State the blood parasite species.
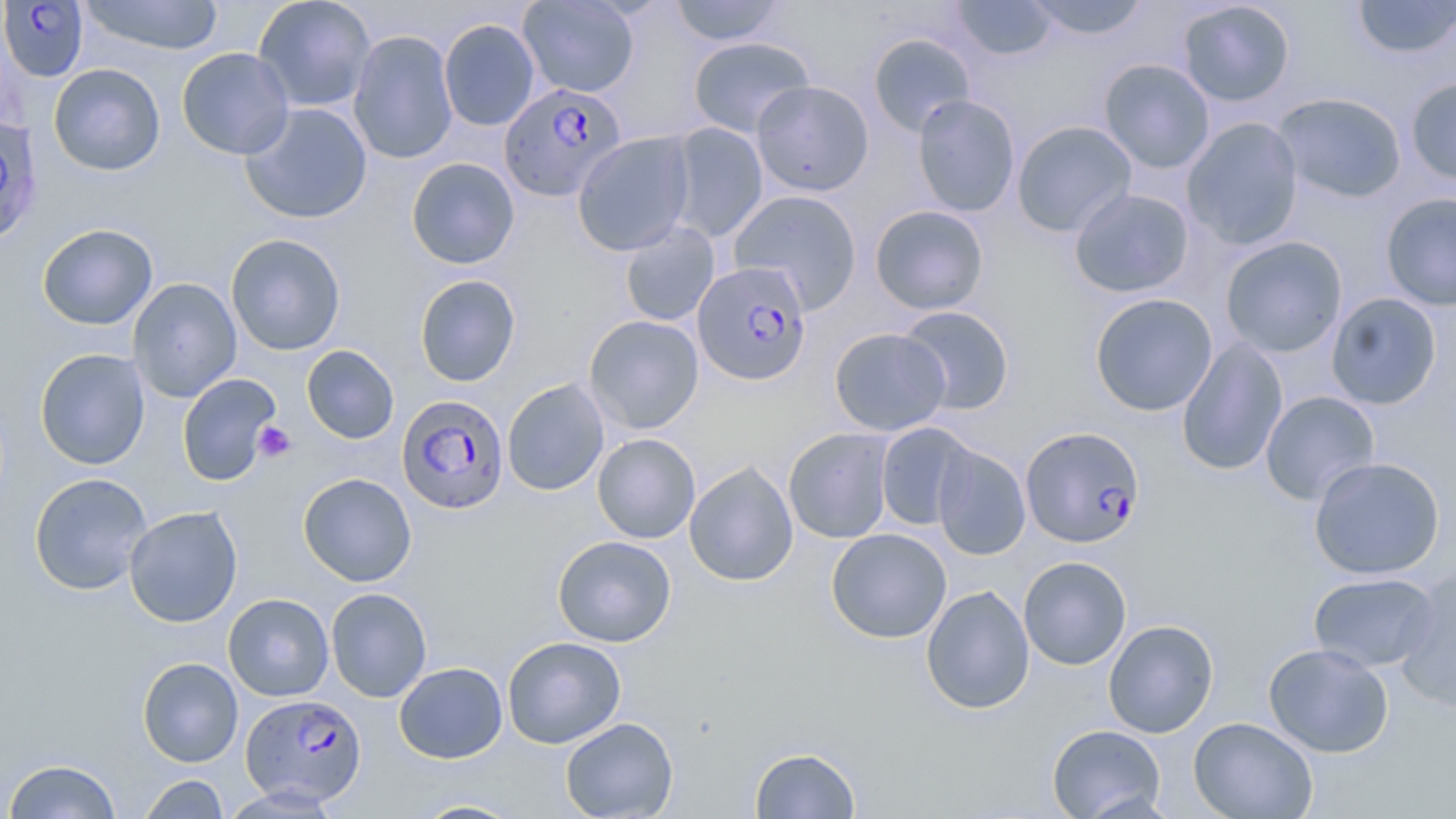

Plasmodium falciparum.

stain = May-Grünwald-Giemsa
uninfected red blood cell locations = approximate bounding boxes as [x1, y1, x2, y2] in pixels: [78, 0, 225, 56], [252, 0, 376, 113], [518, 0, 640, 98], [668, 0, 786, 46], [951, 0, 1058, 62], [1024, 0, 1151, 41], [1352, 0, 1455, 60], [1177, 1, 1296, 107], [439, 18, 540, 131], [348, 30, 459, 165], [868, 33, 976, 138], [687, 36, 815, 138], [176, 47, 295, 160], [1099, 58, 1215, 174], [49, 63, 165, 176], [1405, 77, 1456, 186], [751, 80, 874, 196], [1273, 92, 1408, 203], [911, 94, 1020, 217], [240, 102, 373, 224], [668, 116, 868, 231], [1182, 117, 1304, 250], [1012, 120, 1137, 237], [665, 123, 768, 244], [573, 132, 695, 256], [406, 157, 520, 269], [1069, 187, 1194, 298], [727, 189, 863, 313], [1380, 191, 1456, 312], [870, 204, 989, 315], [619, 220, 720, 327], [37, 223, 158, 330], [225, 233, 346, 356], [1220, 236, 1348, 358], [414, 274, 521, 387], [128, 278, 242, 403], [1325, 292, 1442, 410], [1090, 293, 1218, 416], [897, 305, 1015, 416], [583, 315, 704, 434], [829, 327, 951, 436], [1176, 337, 1288, 476], [301, 345, 399, 444], [34, 348, 150, 469], [177, 373, 282, 485], [502, 378, 610, 496], [1260, 391, 1380, 505], [875, 422, 977, 531], [783, 427, 896, 544], [592, 433, 701, 544], [932, 444, 1031, 561], [1308, 456, 1446, 580], [684, 461, 799, 587], [29, 472, 153, 596], [298, 473, 417, 587], [123, 506, 243, 627], [826, 528, 952, 643], [552, 535, 676, 647], [1018, 556, 1131, 670], [1394, 567, 1456, 714], [1308, 571, 1439, 672], [920, 585, 1035, 714], [326, 587, 432, 703], [223, 593, 334, 701], [1103, 619, 1219, 738], [502, 636, 626, 749], [1263, 643, 1394, 757], [137, 657, 243, 767], [393, 661, 508, 763], [560, 717, 678, 818], [1188, 717, 1317, 819], [1047, 724, 1166, 819], [749, 746, 861, 818], [3, 758, 122, 818], [138, 774, 229, 818], [220, 785, 343, 817], [412, 799, 525, 818]
image size = 1456×819 pixels
field of view = single
modality = optical microscopy
Plasmodium falciparum-infected red blood cell locations = approximate bounding boxes as [x1, y1, x2, y2] in pixels: [1, 0, 89, 82], [499, 84, 628, 204], [0, 116, 44, 249], [693, 260, 812, 386], [397, 395, 509, 514], [1021, 425, 1145, 549], [238, 693, 364, 806]
platelet locations = approximate bounding boxes as [x1, y1, x2, y2] in pixels: [252, 421, 297, 462]
preparation = thin blood film
magnification = 1000x